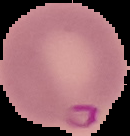

malaria status = parasitized
image size = 130×136 pixels
image type = segmented cell region with the area outside set to black
preparation = thin blood smear